State which parasite is depicted.
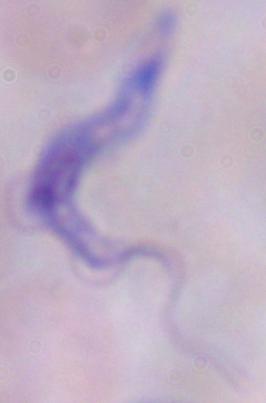

This is a trypanosome.

Photomicrograph. 1000x magnification.